Give a bounding box for every parasitised red blood cell.
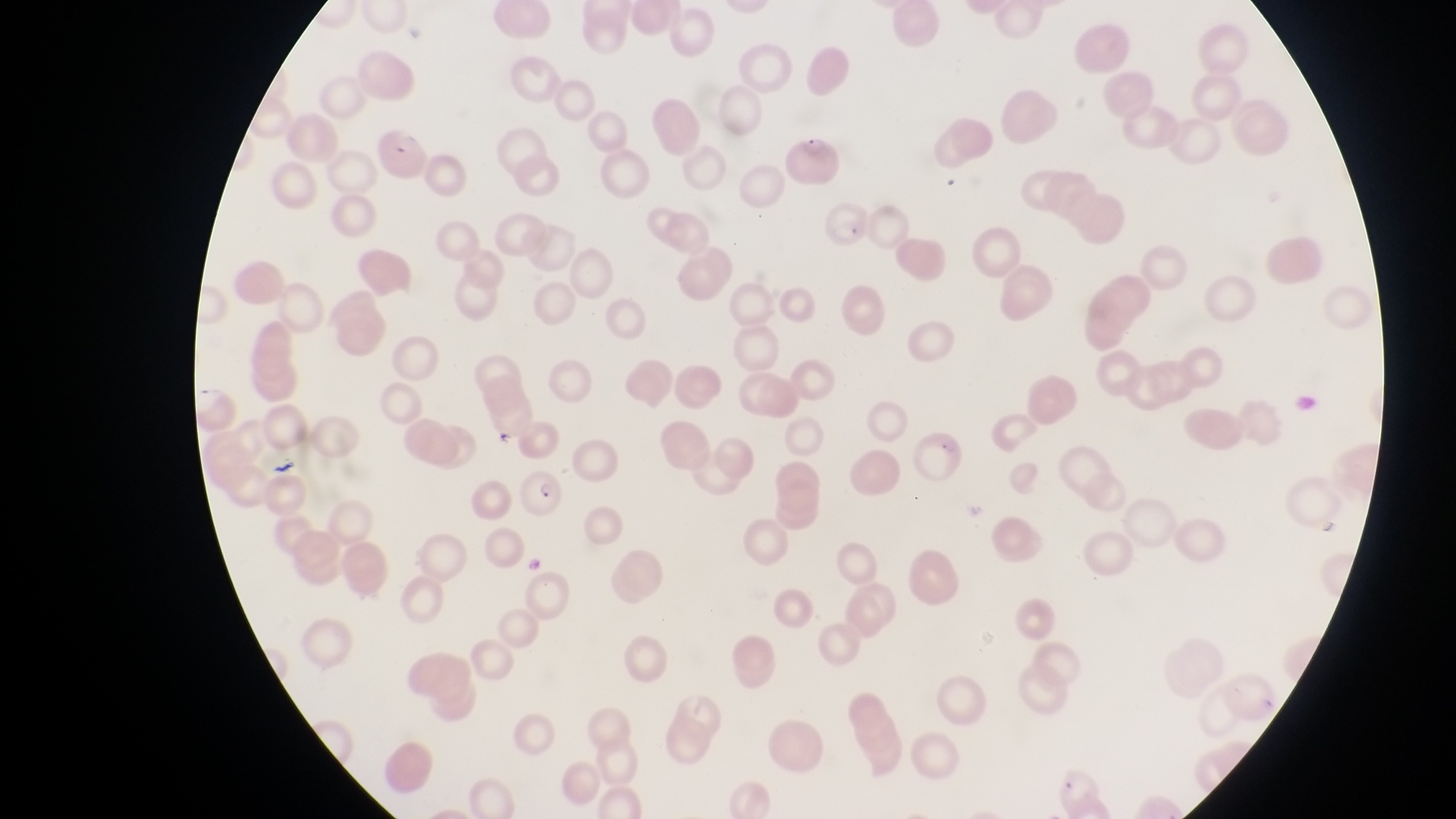
Approximate bounding boxes as left top right bottom in pixels.
Parasitised red blood cells: 376 125 432 180; 785 127 840 183; 825 199 872 257; 518 469 564 518.

Summary:
  - Capture: smartphone photograph through the eyepiece of an Olympus CX-23 microscope
  - Magnification: 1000x
  - Field of view: single
  - Country: Uganda
  - Preparation: thin blood smear
  - Image size: 1456×819 pixels